Identify the parasite.
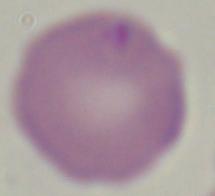
Babesia.

Summary:
  - Magnification: 1000x
  - Modality: photomicrograph